Outline each blood parasite and name the species.
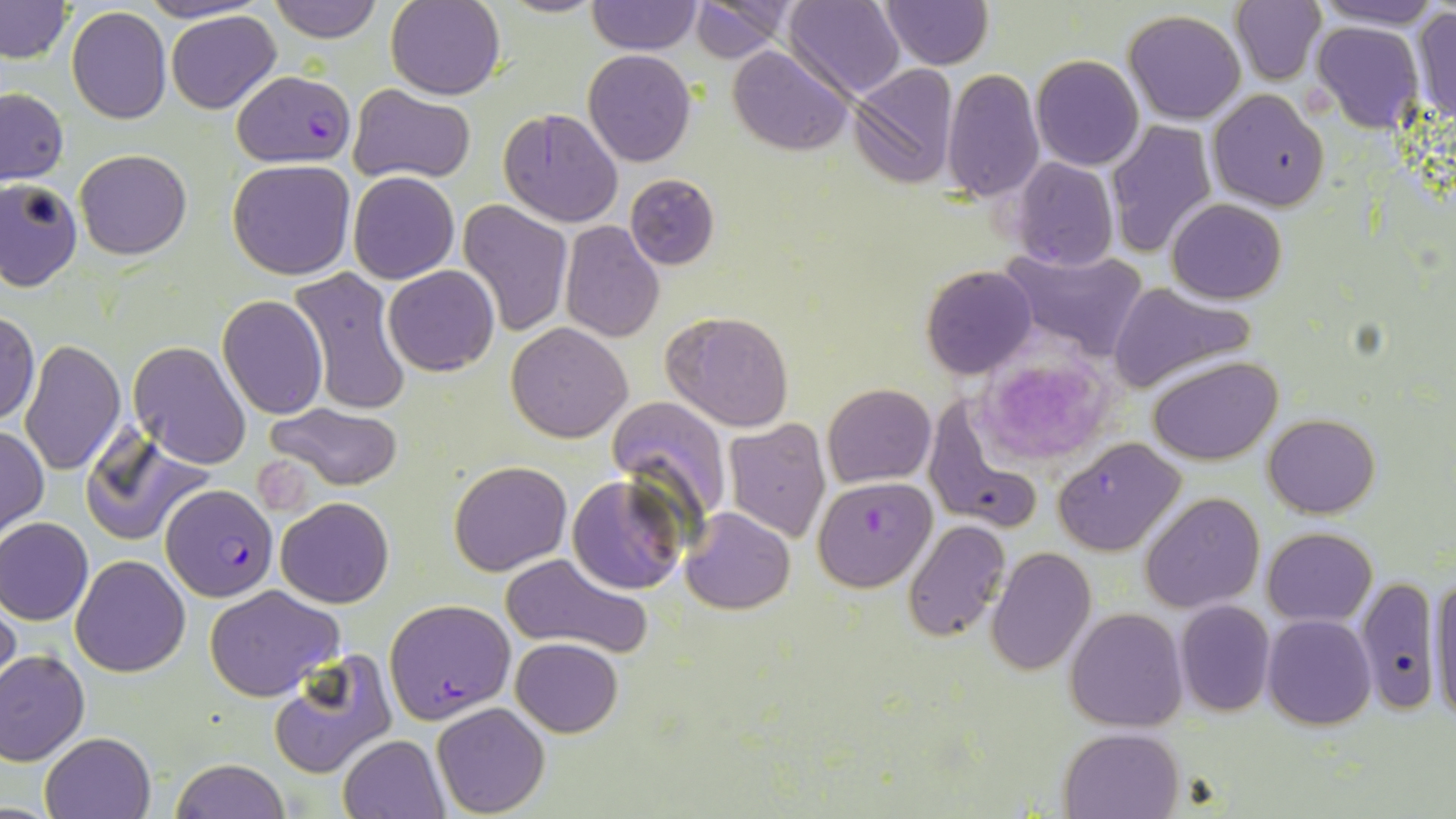

Approximate bounding boxes as [x1, y1, x2, y2] in pixels.
Plasmodium falciparum-infected red blood cells: [231, 69, 355, 165], [812, 476, 937, 591], [161, 484, 277, 604], [384, 599, 516, 722].
No Plasmodium ovale, Plasmodium malariae, Plasmodium vivax, Babesia divergens, or Trypanosoma brucei observed.

Summary:
  - Platelet locations: [977, 352, 1119, 464]
  - Uninfected red blood cell locations: [135, 0, 268, 23], [266, 0, 383, 44], [498, 0, 608, 17], [586, 0, 701, 54], [687, 0, 800, 61], [786, 0, 907, 100], [1231, 0, 1327, 86], [1310, 0, 1445, 29], [0, 1, 73, 64], [386, 1, 506, 100], [881, 2, 993, 69], [65, 7, 171, 124], [1409, 7, 1456, 126], [166, 10, 282, 113], [1123, 10, 1248, 126], [1312, 21, 1426, 135], [728, 44, 852, 154], [583, 49, 698, 166], [966, 51, 1108, 208], [1030, 54, 1143, 171], [848, 64, 961, 189], [941, 68, 1043, 201], [350, 85, 474, 183], [0, 88, 69, 185], [1208, 89, 1330, 211], [499, 107, 623, 228], [1107, 119, 1217, 257], [75, 150, 193, 259], [1011, 157, 1118, 272], [227, 159, 356, 281], [348, 171, 459, 284], [624, 172, 720, 269], [1, 178, 82, 290], [1169, 198, 1287, 303], [458, 200, 573, 336], [560, 220, 664, 341], [1000, 246, 1149, 359], [384, 265, 499, 376], [921, 265, 1037, 379], [288, 267, 412, 417], [1106, 282, 1259, 393], [217, 294, 329, 420], [1, 310, 40, 425], [660, 310, 795, 432], [506, 322, 633, 442], [18, 339, 127, 476], [127, 340, 251, 469], [1148, 355, 1282, 465], [823, 383, 937, 486], [607, 395, 733, 528], [924, 395, 1042, 537], [265, 401, 404, 491], [1264, 413, 1380, 517], [723, 419, 830, 542], [0, 424, 48, 538], [80, 431, 214, 546], [1051, 438, 1185, 556], [447, 461, 573, 575], [567, 474, 686, 594], [1139, 491, 1265, 612], [275, 497, 395, 607], [680, 507, 795, 614], [0, 517, 93, 625], [902, 519, 1010, 641], [1264, 528, 1377, 624], [988, 547, 1095, 676], [71, 554, 192, 677], [498, 554, 653, 659], [1357, 574, 1440, 719], [1427, 574, 1456, 724], [205, 584, 344, 702], [0, 589, 22, 700], [1174, 602, 1275, 717], [1065, 607, 1188, 732], [1262, 614, 1375, 730], [511, 638, 623, 737], [0, 650, 90, 765], [267, 650, 396, 779], [431, 702, 551, 817], [1060, 726, 1184, 818], [40, 731, 154, 819], [338, 734, 449, 819], [170, 758, 291, 818]
  - Slide-level diagnosis: Plasmodium falciparum
  - Field of view: single
  - Image size: 1456×819 pixels
  - Stain: May-Grünwald-Giemsa
  - Modality: light microscopy
  - Magnification: 1000x
  - Preparation: thin blood film